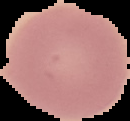
{
  "preparation": "thin blood film",
  "image_size": "130×121 pixels",
  "image_type": "segmented cell region with the area outside set to black",
  "result": "no Plasmodium parasites seen"
}